Give the position of every Plasmodium parasite visible.
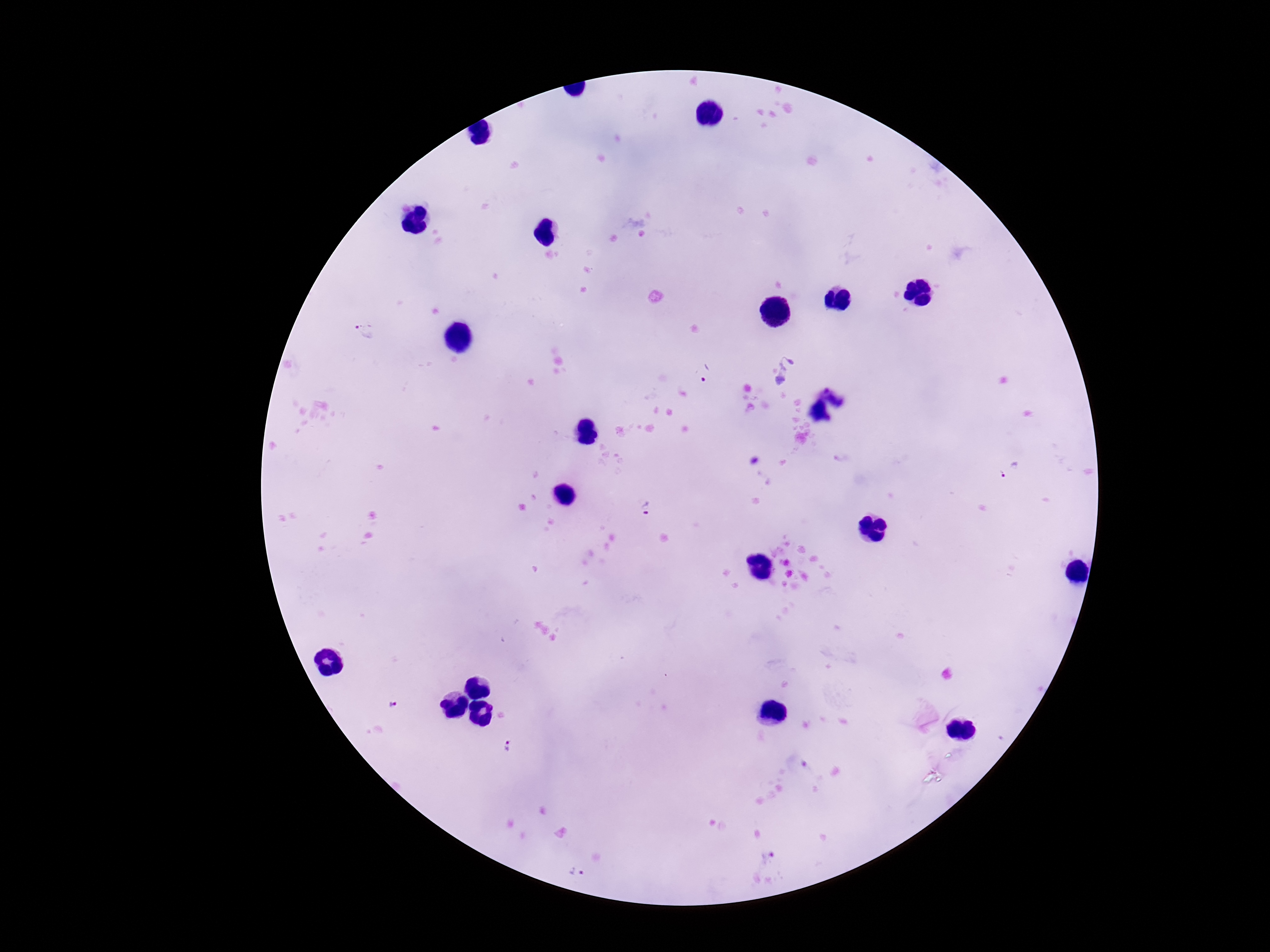
Approximate centers as (x, y) in pixels.
Plasmodium parasites: (364, 331), (706, 373), (1011, 473), (648, 510), (391, 703), (508, 745), (767, 858), (578, 874).

image size = 1270×952 pixels
stain = Giemsa
capture = smartphone camera through the microscope eyepiece
patient malaria status = positive
preparation = thick peripheral-blood smear
field of view = single
magnification = 100x